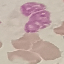 Malaria status: uninfected. Photographed with a smartphone camera at the microscope eyepiece. Cell patch, automatically extracted from a larger field of view and resized to 64 × 64 pixels. Giemsa stain. Thin blood smear.